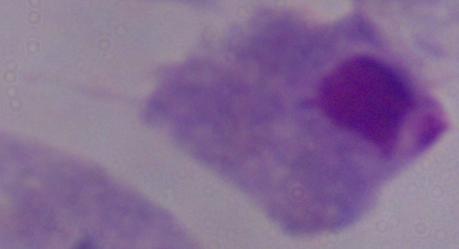
identification = trichomonad
modality = photomicrograph
magnification = 1000x